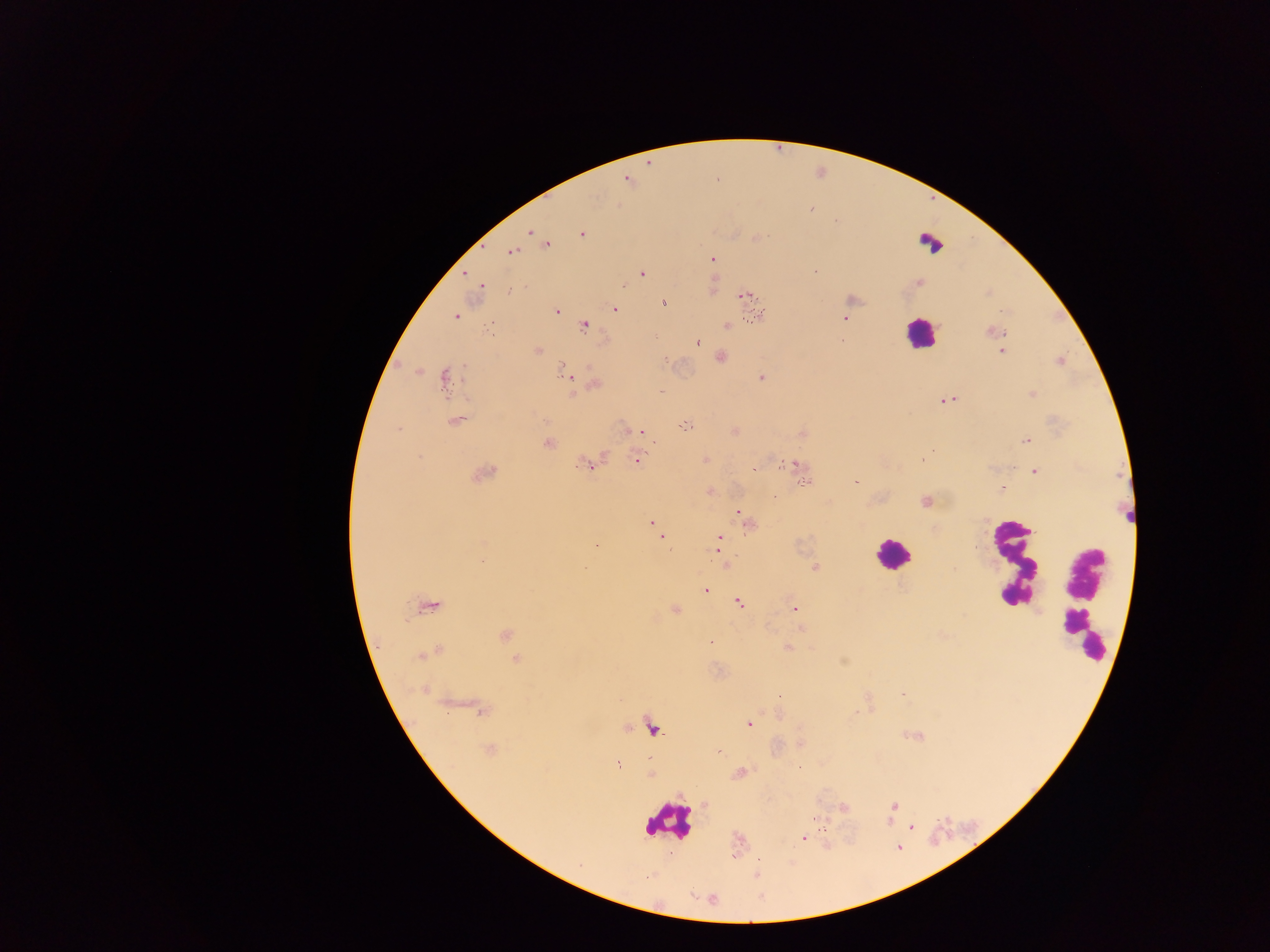
image size = 1270×952 pixels
preparation = thick blood smear
leukocyte locations = approximate centers as (x, y) in pixels: (930, 244), (920, 333), (892, 553), (1012, 562), (1082, 601), (669, 822)
capture = mobile-phone photograph through a microscope
malaria parasite locations = approximate centers as (x, y) in pixels: (626, 179), (810, 208), (530, 231), (581, 234), (756, 238), (546, 244), (511, 252), (712, 259), (815, 271), (642, 274), (480, 286), (510, 290), (745, 295), (664, 304), (615, 309), (557, 310), (758, 315), (455, 317), (844, 319), (585, 326), (726, 326), (490, 327), (994, 331), (698, 342), (537, 350), (1002, 351), (719, 357), (665, 359), (564, 371), (444, 378), (761, 378), (594, 384), (661, 391), (948, 399), (455, 420), (686, 426), (399, 429), (639, 433), (1027, 441), (548, 444), (604, 456), (419, 458), (923, 460), (637, 461), (788, 462), (587, 465), (799, 465), (754, 468), (1034, 472), (484, 473), (806, 482), (856, 482), (1002, 488), (710, 491), (773, 497), (926, 501), (738, 513), (744, 519), (654, 525), (749, 525), (661, 536), (719, 538), (718, 547), (815, 568), (585, 569), (705, 590), (738, 603), (429, 606), (675, 610), (795, 610), (506, 635), (789, 648), (430, 654), (517, 660), (902, 695), (480, 710), (748, 724), (653, 729), (489, 750), (720, 751), (619, 766), (894, 806), (844, 808), (814, 818), (911, 827), (804, 839), (758, 859)
field of view = single
country = Ghana